Assess this cell for malaria.
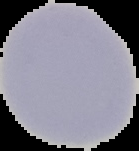
It is uninfected.

image type = segmented cell region with the area outside set to black
preparation = thin blood smear
image size = 139×151 pixels